Name the parasite shown.
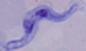
This is a trypanosome.

1000x magnification. Photomicrograph.